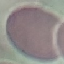

Malaria status: uninfected. Giemsa stain. Thin smear of blood. Automatically extracted cell patch, resized to 64 × 64 pixels. Acquired by smartphone through the microscope eyepiece.